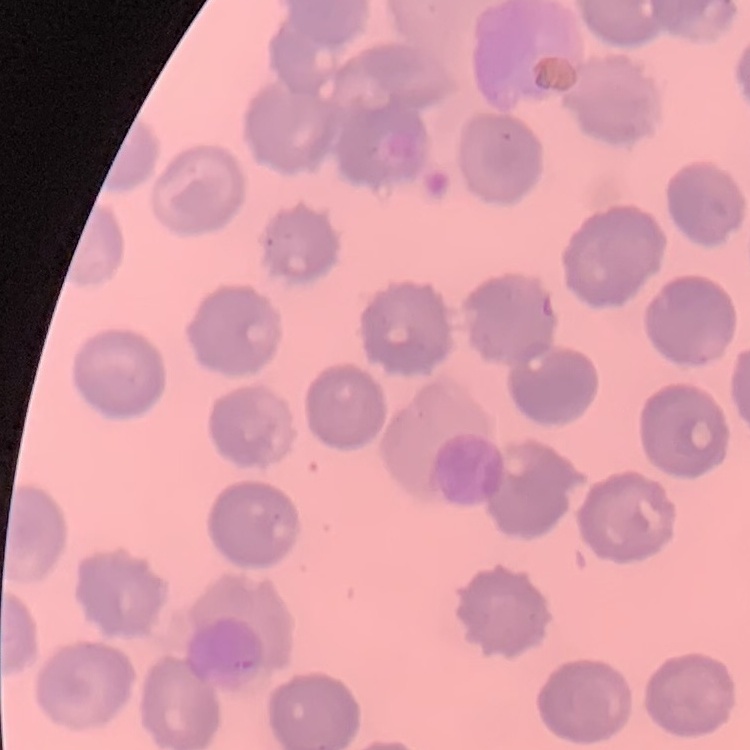
Summary:
  - Red blood cell morphology: no rouleaux formation
  - Image type: square crop of a larger photomicrograph
  - Stain: Field's or Giemsa
  - Preparation: thin peripheral smear